Describe the morphology of the red blood cells.
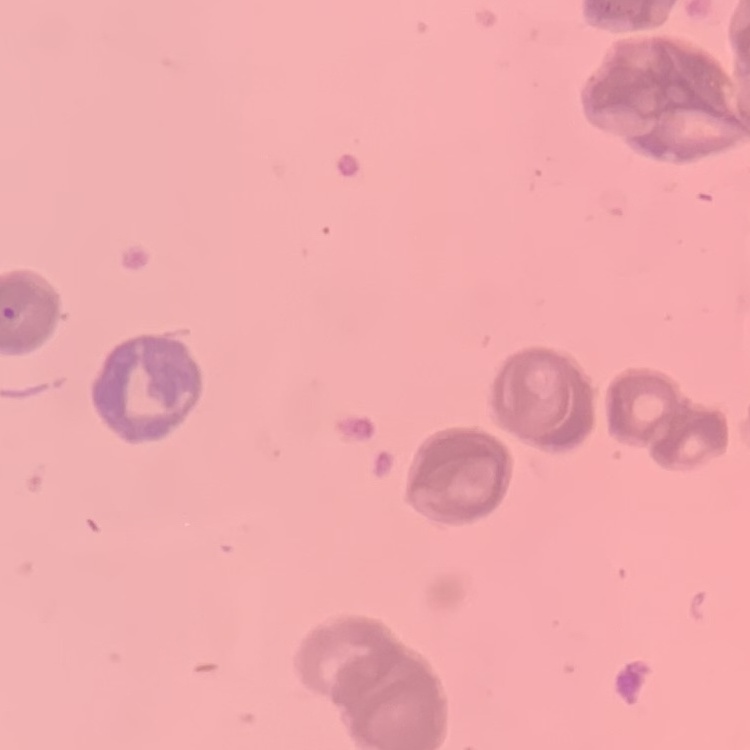

Rouleaux formation.

Summary:
  - Stain: Field's or Giemsa
  - Image type: one tile cut from a larger photomicrograph
  - Preparation: thin blood smear